Give the location of every white blood cell.
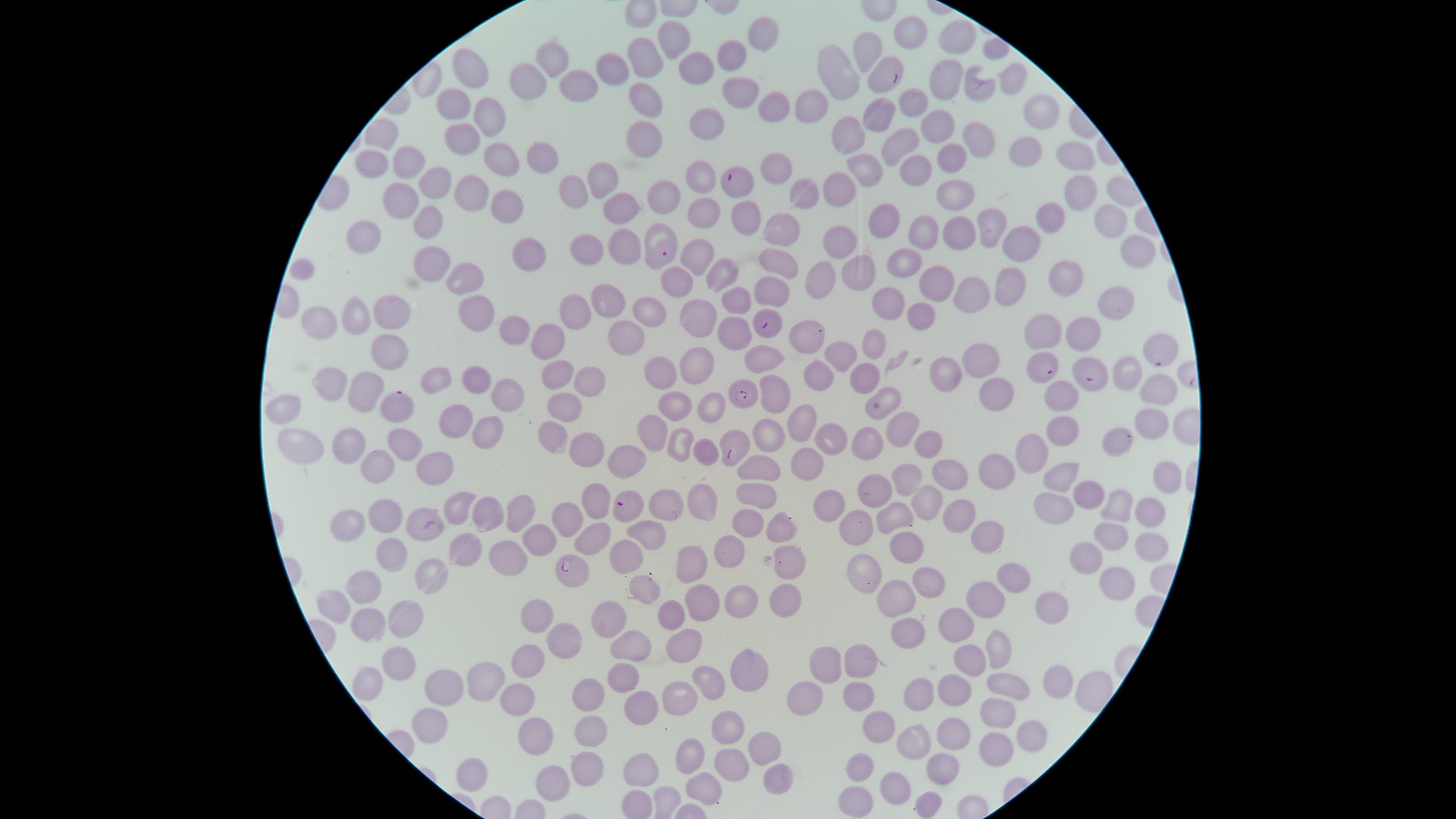
No white blood cells identified.

presence = malaria parasites detected
species = Plasmodium falciparum
uninfected red blood cells = approximate marker points as {x, y} in pixels: {907, 32}, {764, 35}, {674, 39}, {957, 49}, {866, 50}, {647, 57}, {735, 58}, {552, 60}, {615, 67}, {700, 69}, {844, 70}, {472, 73}, {1010, 78}, {581, 79}, {529, 81}, {950, 86}, {743, 94}, {974, 94}, {643, 98}, {911, 102}, {456, 106}, {769, 106}, {813, 108}, {1033, 113}, {874, 114}, {492, 118}, {709, 123}, {938, 125}, {845, 131}, {643, 135}, {899, 138}, {973, 140}, {465, 141}, {1017, 153}, {540, 154}, {950, 155}, {499, 158}, {1070, 160}, {371, 162}, {414, 165}, {870, 169}, {911, 174}, {772, 175}, {699, 177}, {602, 179}, {434, 184}, {843, 187}, {576, 190}, {473, 191}, {799, 194}, {1074, 194}, {958, 195}, {668, 196}, {403, 199}, {502, 204}, {619, 207}, {707, 215}, {743, 218}, {1104, 218}, {881, 219}, {1048, 221}, {428, 223}, {992, 224}, {957, 227}, {928, 231}, {367, 234}, {781, 234}, {849, 243}, {626, 244}, {1025, 244}, {588, 246}, {526, 252}, {1131, 252}, {698, 258}, {427, 260}, {910, 260}, {775, 263}, {303, 271}, {717, 273}, {858, 273}, {468, 277}, {820, 279}, {681, 281}, {1059, 282}, {930, 285}, {1008, 289}, {964, 291}, {606, 298}, {768, 298}, {884, 301}, {735, 303}, {480, 306}, {577, 306}, {1107, 306}, {650, 311}, {389, 314}, {353, 317}, {696, 317}, {921, 323}, {320, 324}, {518, 327}, {1079, 329}, {1044, 334}, {728, 335}, {809, 337}, {618, 338}, {549, 342}, {871, 345}, {843, 354}, {389, 356}, {759, 356}, {989, 357}, {690, 368}, {951, 369}, {555, 372}, {475, 377}, {818, 377}, {660, 378}, {439, 379}, {1124, 379}, {863, 381}, {335, 385}, {586, 385}, {371, 386}, {509, 389}, {773, 392}, {993, 393}, {1155, 394}, {1056, 397}, {286, 404}, {884, 405}, {566, 406}, {714, 406}, {685, 407}, {800, 421}, {448, 422}, {1151, 422}, {904, 425}, {485, 429}, {1061, 430}, {556, 431}, {765, 431}, {651, 432}, {834, 439}, {920, 439}, {863, 441}, {352, 442}, {1114, 442}, {680, 443}, {406, 445}, {311, 446}, {1037, 452}, {585, 453}, {624, 460}, {810, 460}, {381, 463}, {435, 469}, {949, 470}, {761, 471}, {1006, 472}, {914, 474}, {1163, 475}, {1067, 476}, {880, 491}, {757, 492}, {1092, 493}, {598, 498}, {930, 501}, {835, 503}, {1120, 503}, {1057, 506}, {665, 507}, {701, 511}, {963, 514}, {1148, 514}, {460, 515}, {521, 518}, {385, 519}, {485, 519}, {347, 520}, {745, 521}, {893, 522}, {781, 524}, {565, 526}, {425, 527}, {855, 531}, {648, 535}, {990, 535}, {593, 539}, {1109, 539}, {901, 546}, {1147, 546}, {538, 547}, {729, 555}, {390, 556}, {509, 556}, {1080, 556}, {472, 558}, {628, 558}, {694, 559}, {789, 560}, {1017, 575}, {863, 576}, {434, 579}, {930, 580}, {1112, 584}, {372, 586}, {647, 588}, {981, 597}, {780, 598}, {889, 599}, {1057, 599}, {735, 601}, {704, 602}, {339, 604}, {674, 611}, {538, 612}, {614, 617}, {370, 619}, {406, 622}, {955, 624}, {913, 632}, {682, 639}, {565, 643}, {996, 644}, {635, 647}, {860, 657}, {972, 657}, {399, 660}, {823, 667}, {527, 669}, {750, 671}, {367, 681}, {628, 682}, {1054, 683}, {1009, 684}, {708, 685}, {452, 686}, {489, 686}, {958, 688}, {856, 694}, {922, 694}, {588, 696}, {804, 697}, {677, 698}, {515, 705}, {640, 708}, {996, 712}, {432, 726}, {888, 726}, {726, 730}, {589, 731}, {951, 733}, {539, 735}, {1027, 736}, {911, 744}, {760, 745}, {995, 750}, {692, 757}, {862, 767}, {734, 768}, {647, 770}, {585, 771}, {945, 771}, {778, 776}, {557, 781}, {894, 786}, {701, 791}, {855, 801}, {925, 805}
capture = smartphone photograph through the microscope eyepiece
visible region = circular
parasitized red blood cells = approximate marker points as {x, y} in pixels: {889, 72}, {735, 182}, {665, 245}, {765, 322}, {1160, 351}, {1046, 366}, {1092, 375}, {742, 393}, {395, 403}, {736, 448}, {627, 507}, {569, 573}
stain = Giemsa
image size = 1456×819 pixels
preparation = thin blood film
field of view = single